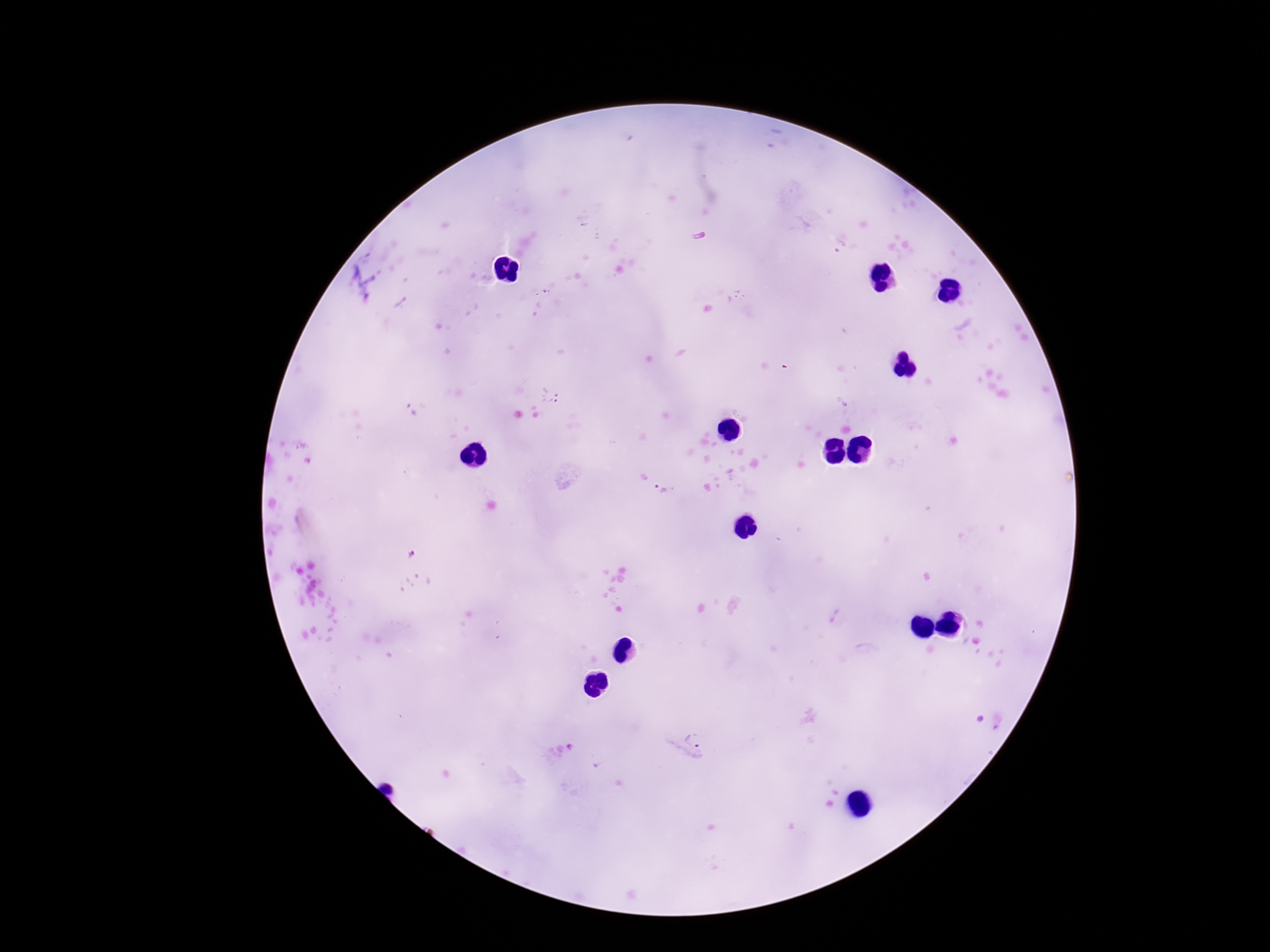

preparation = thick blood film
magnification = 100x
patient malaria status = infected
Plasmodium parasite locations = approximate object centers, in pixels from the top-left corner: (x=840, y=247), (x=551, y=395), (x=409, y=409), (x=661, y=490), (x=687, y=743)
stain = Giemsa
image size = 1270×952 pixels
field of view = one from this slide
capture = smartphone camera through the microscope eyepiece